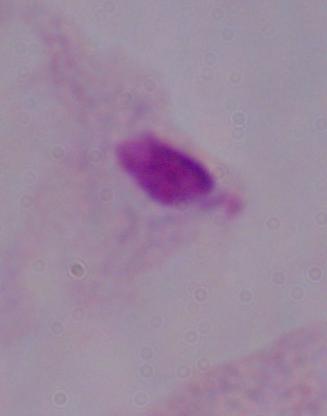

magnification = 1000x
modality = micrograph
identification = trichomonad